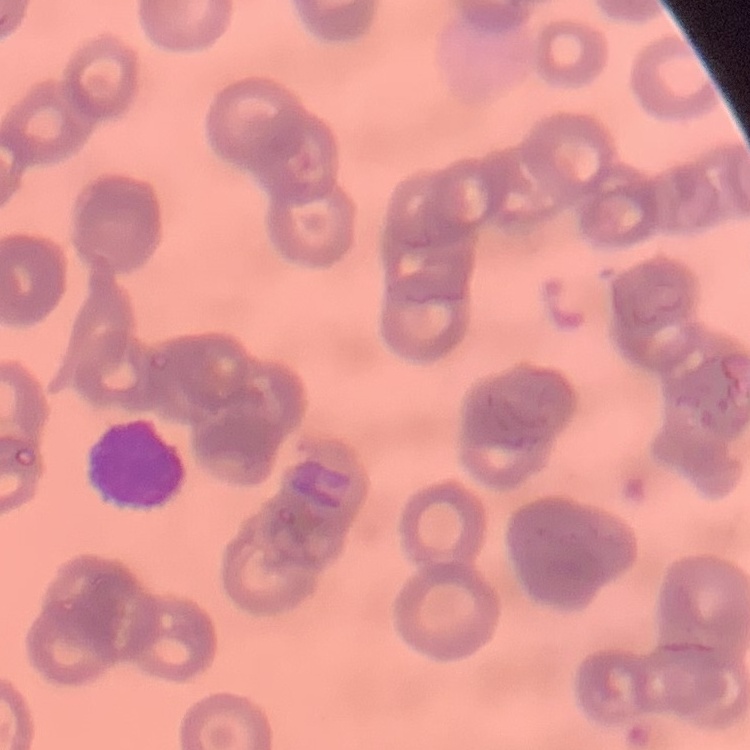
Summary:
  - Red blood cell morphology: rouleaux formation
  - Preparation: thin peripheral smear
  - Image type: one tile cut from a larger photomicrograph
  - Stain: Field's or Giemsa